Name the parasite shown.
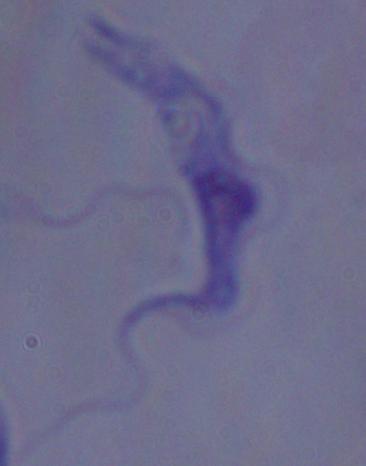

This is a trypanosome.

Summary:
  - Magnification: 1000x
  - Modality: photomicrograph